Report the malaria status of this cell.
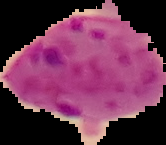

Parasitized.

preparation = thin blood smear
image size = 166×145 pixels
image type = cell region segmented out of the field of view; surrounding area masked to black